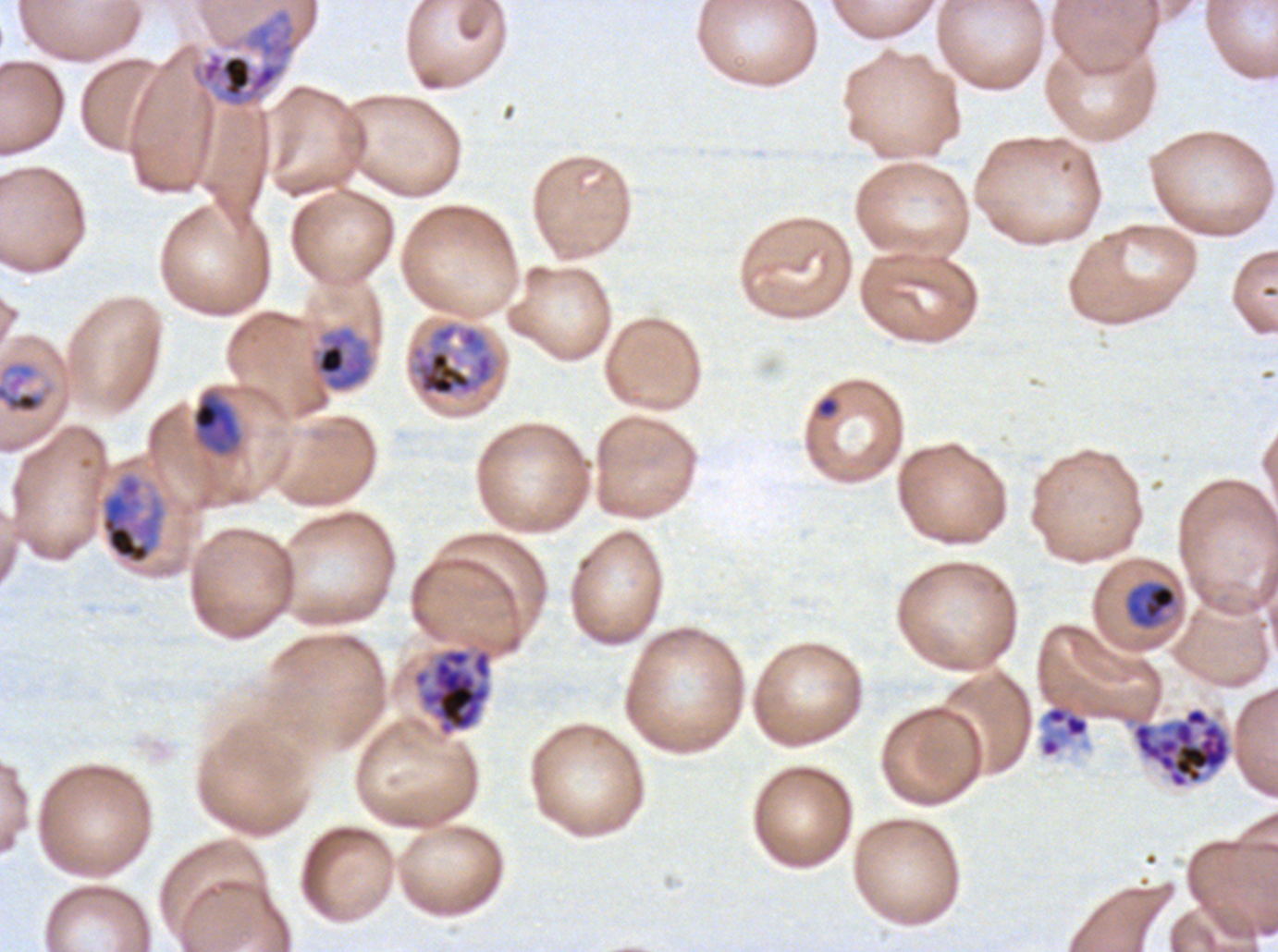

Approximate bounding boxes as {x1, y1, x2, y2} in pixels. Late trophozoite locations: {99, 470, 167, 566}. Early schizont locations: {190, 7, 298, 108}. Late schizont locations: {411, 322, 496, 397}, {412, 647, 493, 737}. Mid trophozoite locations: {313, 326, 372, 392}, {0, 357, 57, 417}, {191, 390, 241, 456}, {1124, 580, 1178, 629}, {1038, 701, 1090, 759}. Late-ring/early-trophozoite locations: {816, 396, 839, 418}. Segmenter locations: {1131, 706, 1232, 789}. Life-cycle stages observed: late-ring/early-trophozoite, mid trophozoite, late trophozoite, early schizont, late schizont, segmenter. Plasmodium falciparum cultured ex vivo for 24 to 48 hours, from a patient in The Gambia. Giemsa stain. A sub-image separated from a larger composite. Thin blood film. Image is 1278×952 pixels.